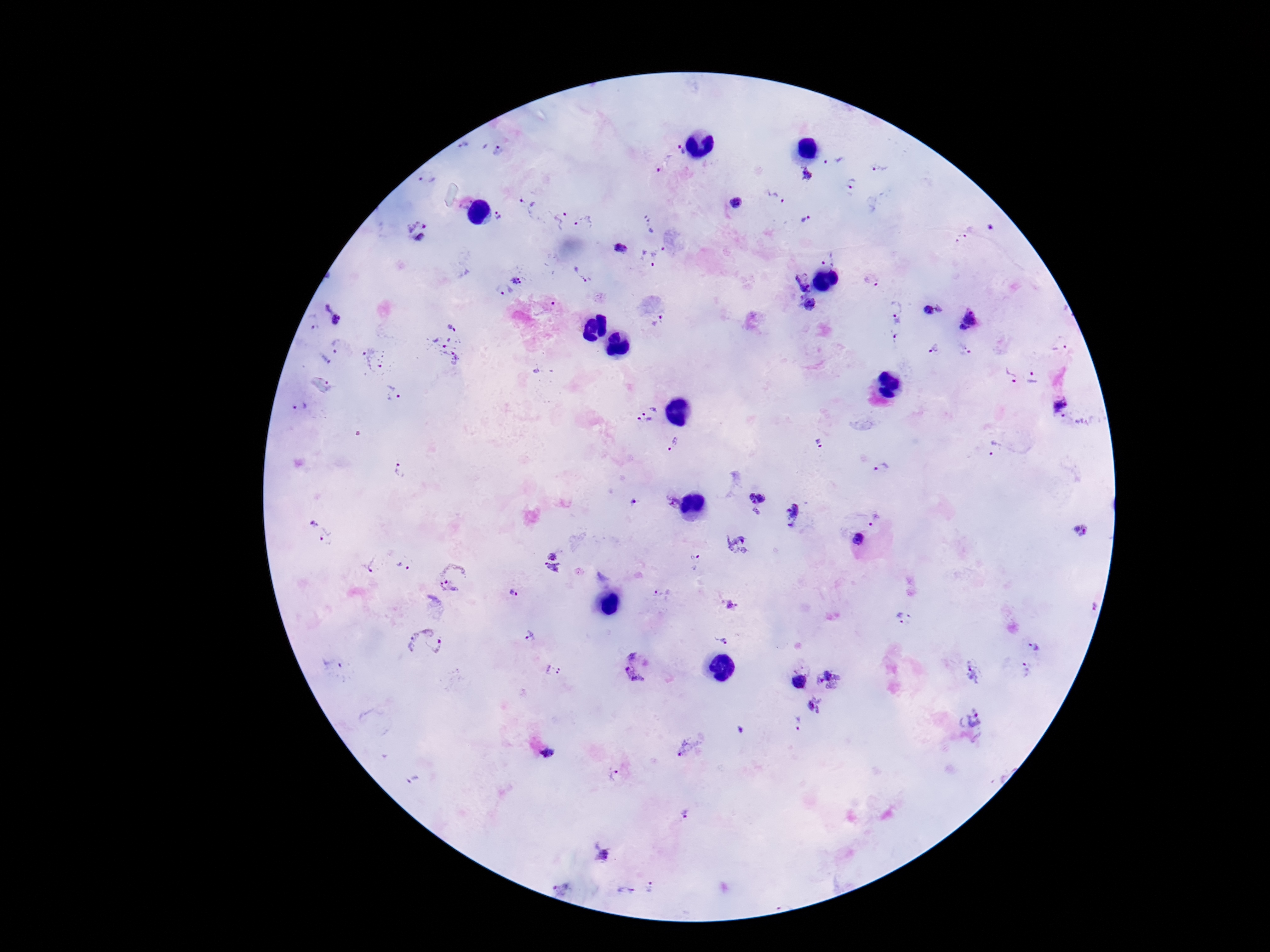
Approximate centers as [x, y] in pixels.
Summary:
  - Plasmodium parasite locations: [463, 144], [682, 151], [499, 152], [833, 161], [664, 167], [880, 168], [808, 176], [430, 177], [852, 183], [776, 198], [526, 207], [496, 217], [558, 218], [808, 220], [585, 222], [651, 225], [418, 229], [961, 239], [620, 246], [652, 254], [828, 257], [580, 274], [518, 277], [872, 279], [800, 282], [502, 290], [811, 304], [894, 306], [940, 309], [928, 310], [335, 311], [971, 315], [659, 322], [314, 325], [962, 328], [897, 331], [448, 343], [1060, 343], [341, 347], [935, 350], [964, 350], [375, 360], [325, 361], [1009, 375], [1034, 377], [323, 385], [394, 395], [304, 408], [1063, 408], [648, 411], [818, 443], [674, 444], [996, 449], [399, 467], [882, 468], [758, 500], [673, 501], [632, 502], [794, 516], [874, 518], [1081, 530], [320, 531], [858, 540], [737, 546], [552, 556], [695, 563], [373, 565], [404, 567], [552, 570], [453, 578], [513, 594], [664, 595], [1094, 605], [730, 607], [903, 620], [529, 637], [723, 638], [424, 643], [1034, 648], [335, 664], [636, 666], [1028, 669], [553, 671], [972, 673], [828, 680], [798, 681], [814, 705], [975, 720], [798, 724], [687, 748], [547, 752], [615, 776], [415, 780], [685, 814], [604, 854], [651, 888], [562, 889], [625, 891]
  - Patient malaria status: infected
  - Field of view: single
  - Preparation: thick blood film
  - Stain: Giemsa
  - Capture: smartphone camera through the microscope eyepiece
  - Magnification: 100x
  - Image size: 1270×952 pixels